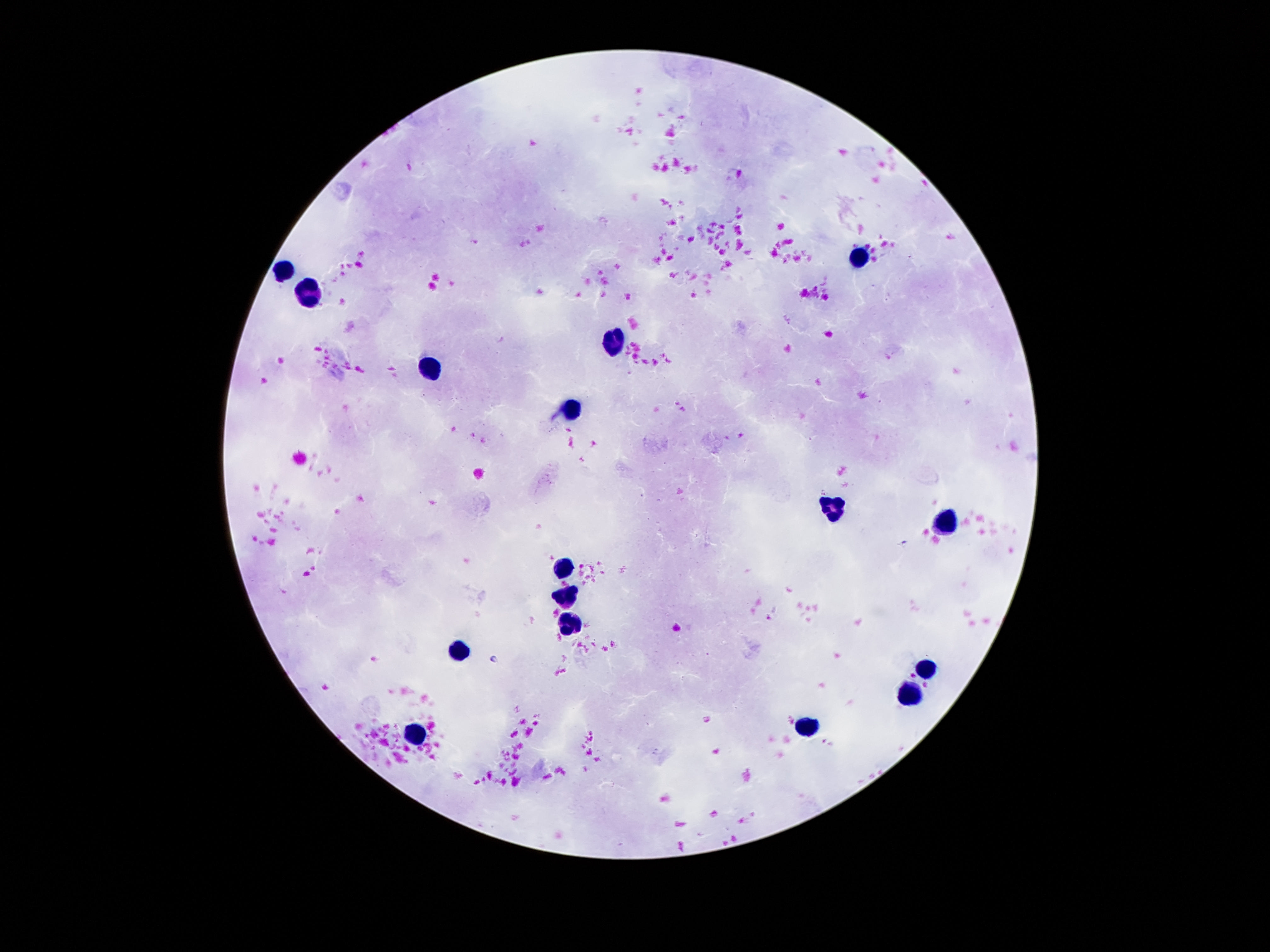
preparation = thick blood smear
leukocyte locations = approximate centers as [x, y] in pixels: [862, 255], [280, 268], [311, 293], [608, 345], [429, 369], [574, 410], [832, 507], [941, 522], [561, 564], [566, 595], [570, 621], [458, 652], [925, 669], [910, 693], [807, 725], [412, 733]
field of view = single
capture = smartphone camera through the microscope eyepiece
stain = Giemsa
patient malaria status = uninfected
magnification = 100x
image size = 1270×952 pixels